Assess the morphology of the erythrocytes.
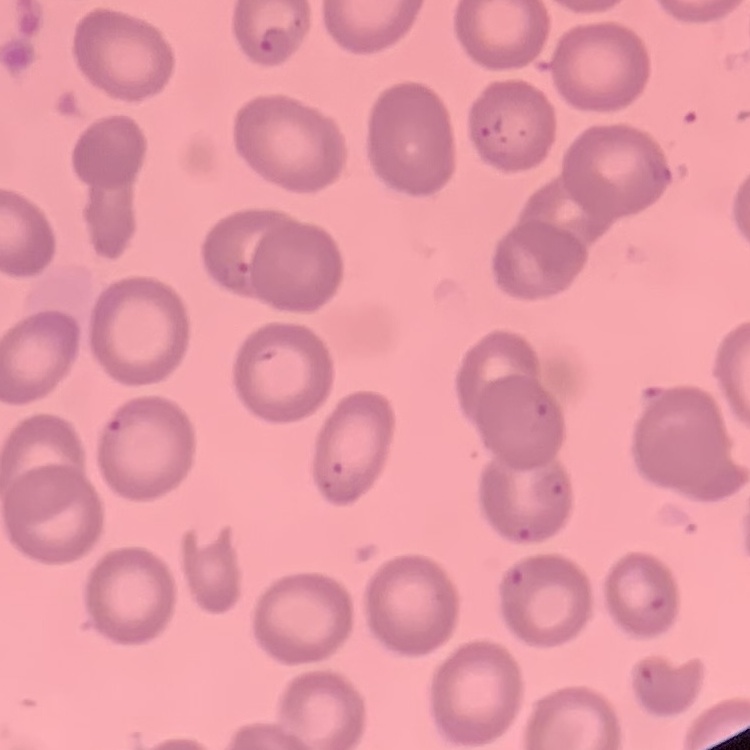

No rouleaux formation.

Summary:
  - Stain: Field's or Giemsa
  - Preparation: thin blood film
  - Image type: square crop of a larger photomicrograph